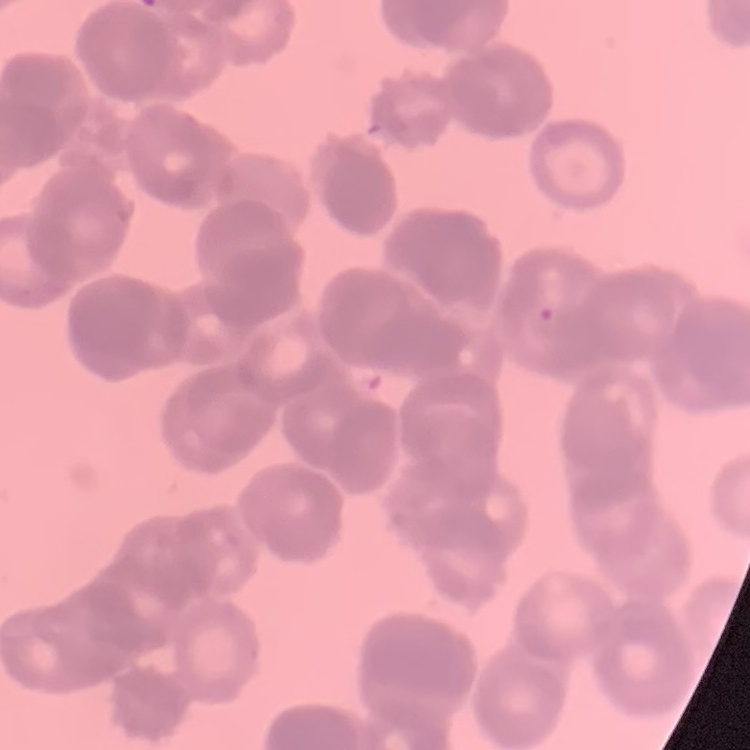
The red blood cells exhibit rouleaux formation. One tile cut from a larger photomicrograph. Thin peripheral smear. Stained with either Field's or Giemsa.